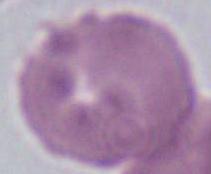

Micrograph. A red blood cell is seen. Captured at 1000x magnification.